Report the malaria status of this cell.
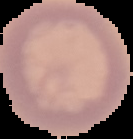

Uninfected.

image size = 133×139 pixels
preparation = thin blood film
image type = segmented cell region on a black background